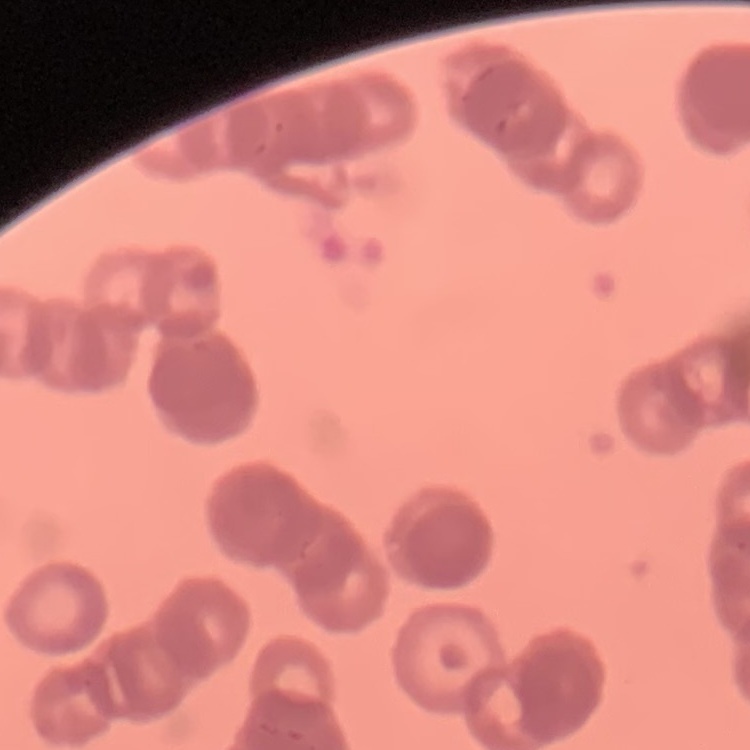
red_blood_cell_morphology: rouleaux formation
stain: Field's or Giemsa
preparation: thin blood film
image_type: one tile cut from a larger photomicrograph